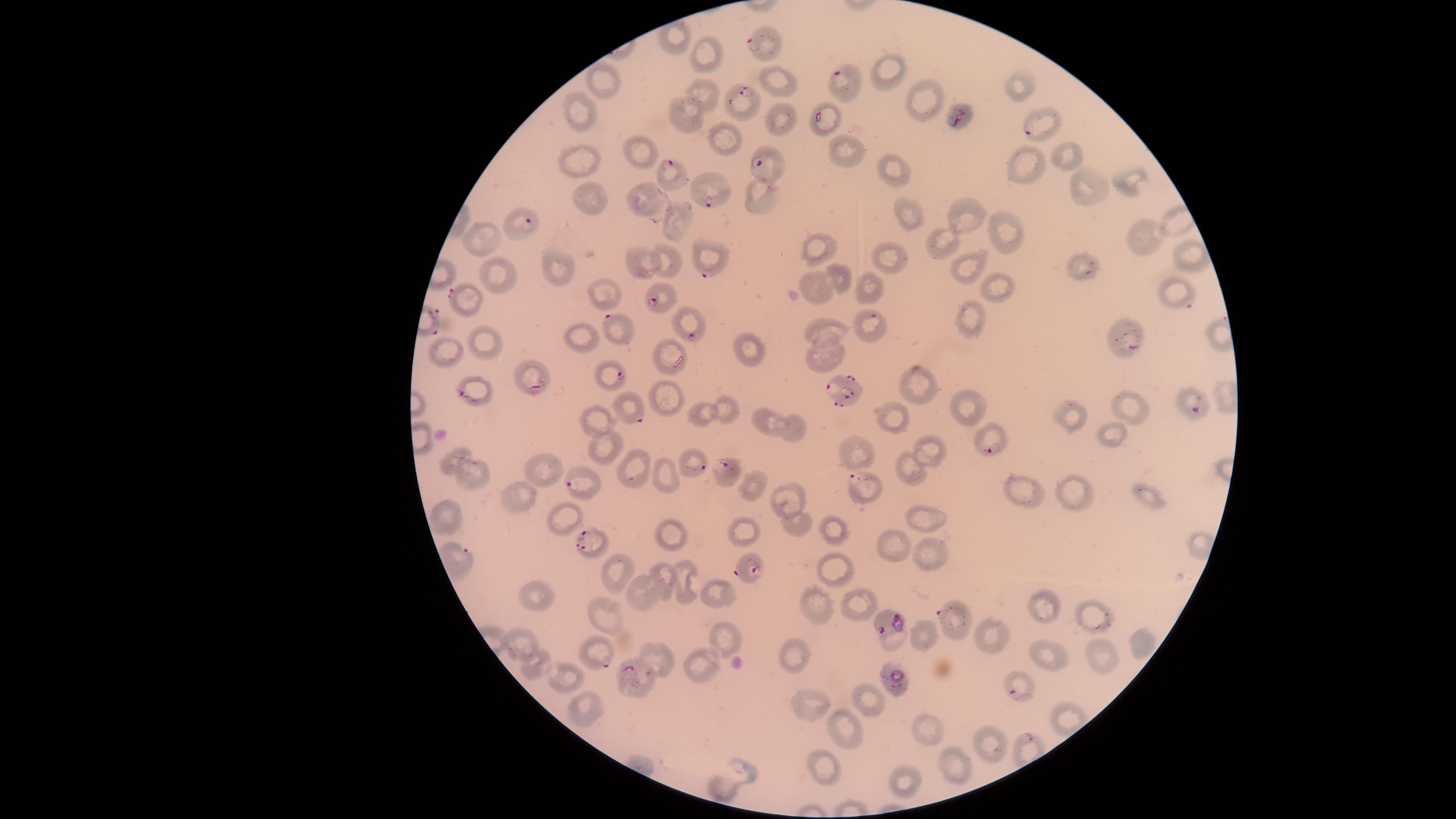

Approximate marker points as [x, y] in pixels. Parasitized red blood cells: [751, 41], [840, 71], [743, 95], [958, 117], [1031, 132], [669, 165], [756, 166], [713, 205], [527, 223], [1091, 264], [710, 272], [455, 293], [654, 304], [1187, 304], [873, 316], [610, 320], [694, 332], [1133, 347], [617, 374], [539, 386], [846, 391], [462, 395], [1194, 407], [640, 420], [993, 447], [729, 465], [695, 470], [853, 478], [577, 485], [587, 542], [751, 570], [943, 614], [895, 623], [603, 660], [629, 669], [897, 681], [1015, 696]. Uninfected red blood cells: [710, 52], [881, 74], [1021, 79], [778, 80], [607, 84], [703, 99], [919, 101], [578, 112], [686, 116], [781, 120], [725, 139], [632, 148], [843, 152], [1073, 153], [577, 160], [1022, 162], [889, 169], [1130, 180], [641, 194], [758, 194], [1091, 195], [595, 205], [911, 213], [967, 218], [677, 222], [1147, 232], [491, 235], [1012, 235], [946, 242], [822, 243], [1188, 257], [641, 261], [669, 262], [890, 262], [971, 266], [563, 269], [838, 277], [499, 278], [870, 288], [1002, 289], [819, 292], [605, 293], [968, 321], [827, 329], [581, 337], [484, 340], [751, 348], [451, 353], [671, 353], [827, 354], [925, 382], [1133, 395], [668, 396], [976, 408], [725, 409], [702, 414], [892, 415], [1075, 416], [598, 419], [771, 419], [795, 426], [1117, 436], [603, 446], [855, 450], [935, 450], [465, 451], [547, 465], [637, 467], [910, 467], [665, 473], [471, 476], [753, 485], [1023, 488], [521, 492], [1079, 492], [1144, 494], [786, 497], [454, 516], [926, 517], [566, 518], [746, 521], [796, 523], [832, 525], [680, 537], [894, 543], [929, 555], [833, 567], [614, 574], [665, 576], [684, 576], [646, 592], [721, 594], [534, 596], [819, 605], [857, 606], [1046, 606], [601, 614], [1095, 615], [724, 634], [926, 636], [996, 636], [518, 637], [1139, 638], [1050, 651], [1105, 652], [797, 654], [662, 656], [534, 664], [700, 668], [570, 679], [595, 699], [871, 702], [810, 706], [840, 726], [928, 729], [992, 739], [955, 766], [746, 770], [832, 771], [906, 778], [724, 786]. Single field of view. Image is 1456×819 pixels. Presence: malaria parasites seen. Thin blood smear. Photographed with a smartphone camera through the microscope eyepiece. Giemsa stain. Species: Plasmodium falciparum. The visible region is circular.